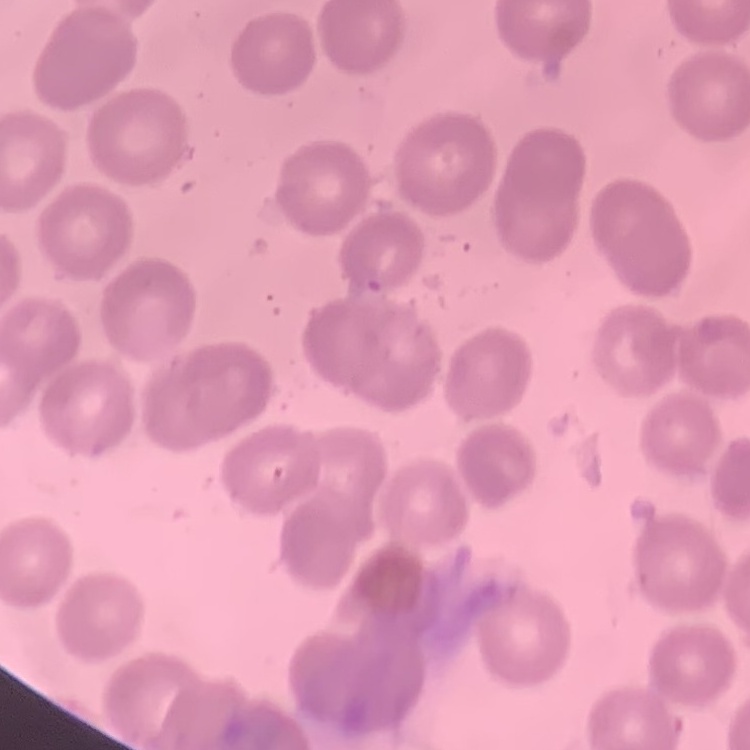
erythrocyte morphology = no rouleaux formation
preparation = thin blood film
image type = square crop of a larger photomicrograph
stain = Field's or Giemsa